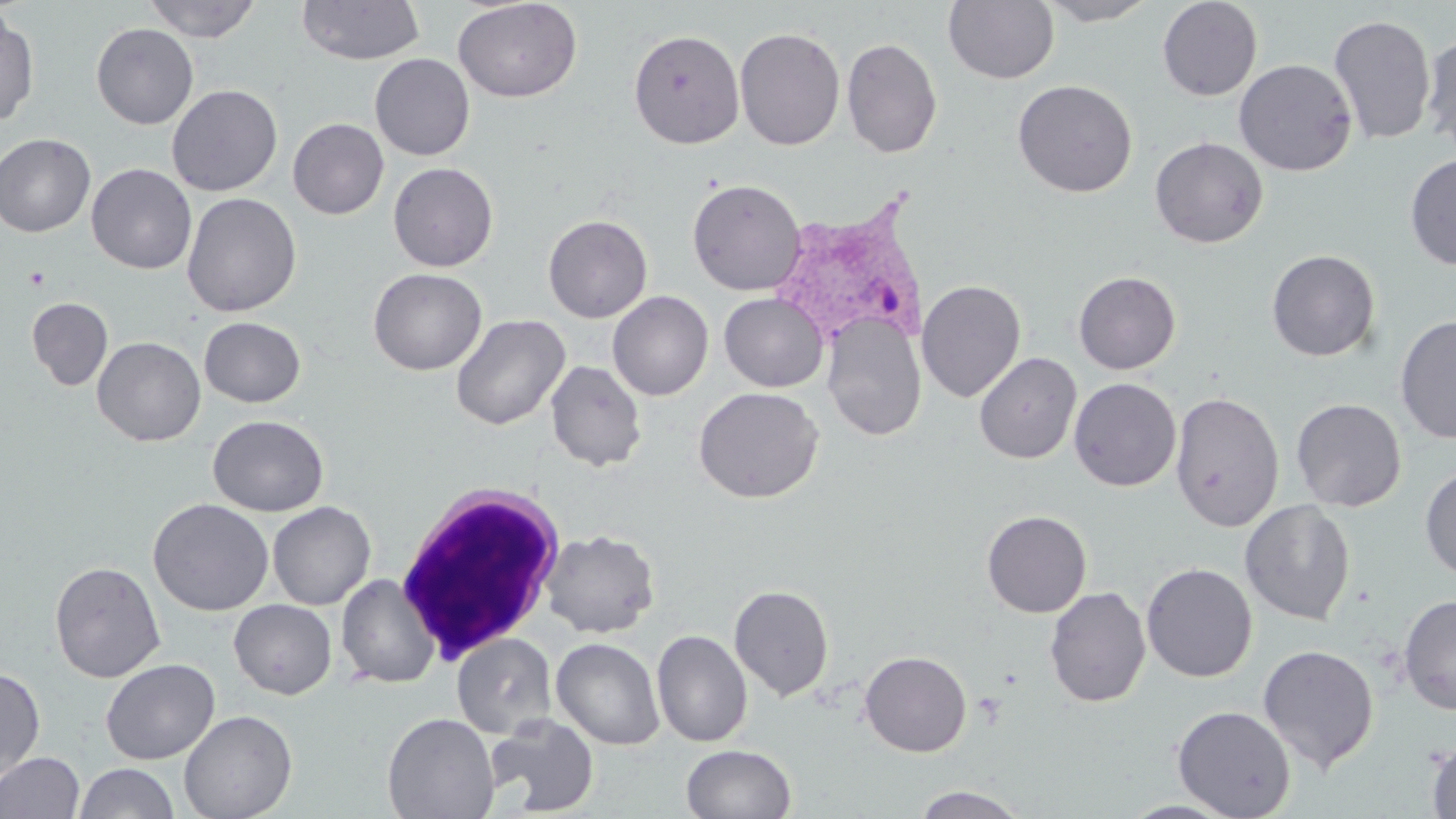
Approximate bounding boxes as [x1, y1, x2, y2] in pixels. Uninfected red blood cell locations: [142, 0, 262, 42], [296, 0, 425, 65], [452, 0, 583, 103], [943, 0, 1059, 85], [1036, 0, 1160, 26], [1157, 0, 1262, 101], [0, 12, 39, 127], [1328, 13, 1437, 146], [91, 23, 199, 129], [734, 26, 845, 151], [629, 29, 746, 149], [1422, 31, 1456, 155], [841, 37, 943, 159], [369, 53, 475, 160], [1234, 58, 1357, 176], [1012, 79, 1137, 198], [167, 84, 283, 196], [288, 118, 389, 219], [0, 133, 96, 237], [1149, 136, 1269, 248], [1404, 153, 1456, 269], [387, 162, 498, 272], [86, 163, 197, 274], [687, 178, 807, 296], [181, 192, 302, 317], [543, 214, 653, 323], [1265, 249, 1381, 362], [369, 268, 487, 375], [1073, 271, 1181, 374], [916, 279, 1026, 402], [607, 290, 714, 400], [719, 292, 828, 392], [26, 297, 113, 390], [451, 313, 571, 431], [822, 314, 926, 441], [1395, 314, 1456, 445], [199, 316, 306, 408], [92, 336, 206, 446], [974, 351, 1082, 464], [545, 360, 647, 472], [1068, 377, 1182, 491], [693, 386, 824, 503], [1169, 390, 1285, 532], [1291, 398, 1407, 512], [207, 415, 329, 517], [1419, 464, 1456, 581], [148, 498, 274, 616], [1239, 499, 1356, 625], [267, 501, 376, 610], [981, 510, 1091, 618], [540, 529, 660, 638], [49, 561, 166, 682], [1141, 562, 1258, 682], [335, 573, 440, 689], [729, 584, 834, 701], [1044, 586, 1151, 707], [1397, 593, 1456, 715], [229, 599, 337, 699], [652, 629, 752, 747], [451, 633, 556, 738], [551, 637, 665, 750], [1258, 643, 1379, 772], [859, 650, 972, 757], [101, 658, 220, 765], [0, 666, 45, 784], [1172, 705, 1296, 818], [179, 709, 298, 819], [382, 712, 500, 819], [486, 714, 600, 816], [1425, 738, 1456, 819], [681, 744, 797, 819], [0, 751, 85, 818], [74, 762, 181, 819], [910, 785, 1032, 818], [1118, 799, 1242, 818]. Plasmodium vivax-infected red blood cell locations: [779, 198, 949, 342]. White blood cell locations: [394, 481, 567, 664]. Platelet locations: [24, 267, 49, 290]. Slide-level diagnosis: Plasmodium vivax. Captured at 1000x magnification. Thin blood film. May-Grünwald-Giemsa stain. Image is 1456×819 pixels. One field of a larger specimen. Light microscopy.